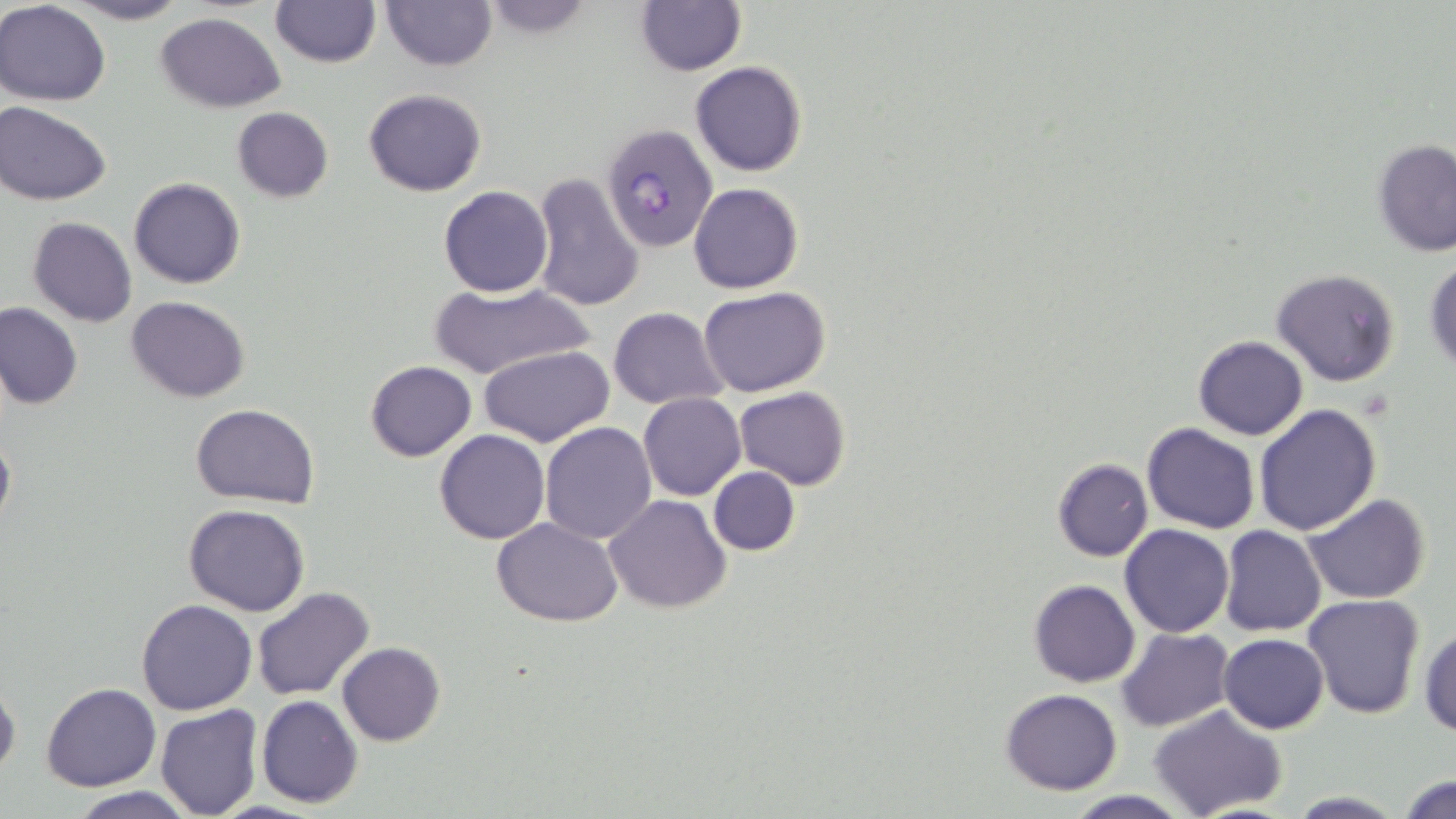

slide_level_diagnosis: Plasmodium falciparum
modality: optical microscopy
stain: May-Grünwald-Giemsa
preparation: thin blood smear
field_of_view: one of a larger specimen
uninfected_red_blood_cell_locations: 'approximate bounding boxes as named x1/y1/x2/y2 corners in pixels: (x1=64, y1=0, x2=191, y2=25), (x1=381, y1=0, x2=496, y2=70), (x1=1, y1=1, x2=113, y2=105), (x1=269, y1=1, x2=379, y2=68), (x1=634, y1=1, x2=746, y2=76), (x1=472, y1=2, x2=603, y2=37), (x1=155, y1=11, x2=287, y2=112), (x1=690, y1=61, x2=807, y2=176), (x1=364, y1=88, x2=487, y2=196), (x1=0, y1=101, x2=111, y2=205), (x1=231, y1=107, x2=333, y2=204), (x1=1372, y1=139, x2=1456, y2=256), (x1=530, y1=173, x2=644, y2=312), (x1=129, y1=177, x2=246, y2=289), (x1=688, y1=183, x2=804, y2=294), (x1=439, y1=186, x2=552, y2=297), (x1=26, y1=217, x2=137, y2=327), (x1=1424, y1=255, x2=1456, y2=375), (x1=1270, y1=268, x2=1402, y2=387), (x1=425, y1=281, x2=599, y2=381), (x1=699, y1=285, x2=832, y2=397), (x1=127, y1=295, x2=250, y2=402), (x1=0, y1=304, x2=83, y2=408), (x1=608, y1=307, x2=727, y2=409), (x1=1192, y1=335, x2=1308, y2=440), (x1=480, y1=344, x2=615, y2=448), (x1=364, y1=360, x2=477, y2=460), (x1=735, y1=386, x2=851, y2=490), (x1=638, y1=392, x2=746, y2=501), (x1=190, y1=403, x2=321, y2=507), (x1=1253, y1=405, x2=1382, y2=536), (x1=539, y1=422, x2=656, y2=543), (x1=1141, y1=423, x2=1261, y2=533), (x1=435, y1=429, x2=551, y2=544), (x1=0, y1=431, x2=15, y2=532), (x1=1053, y1=459, x2=1154, y2=561), (x1=707, y1=466, x2=800, y2=556), (x1=603, y1=493, x2=732, y2=613), (x1=1303, y1=493, x2=1432, y2=604), (x1=185, y1=504, x2=310, y2=616), (x1=492, y1=517, x2=623, y2=625), (x1=1120, y1=523, x2=1234, y2=636), (x1=1218, y1=526, x2=1326, y2=637), (x1=1030, y1=580, x2=1140, y2=687), (x1=253, y1=587, x2=375, y2=699), (x1=1302, y1=594, x2=1427, y2=720), (x1=137, y1=599, x2=256, y2=715), (x1=1419, y1=624, x2=1455, y2=738), (x1=1117, y1=628, x2=1234, y2=730), (x1=1218, y1=633, x2=1328, y2=733), (x1=337, y1=642, x2=445, y2=747), (x1=0, y1=680, x2=20, y2=779), (x1=42, y1=683, x2=161, y2=792), (x1=1000, y1=687, x2=1123, y2=795), (x1=256, y1=694, x2=363, y2=809), (x1=154, y1=703, x2=265, y2=819), (x1=1149, y1=705, x2=1289, y2=819), (x1=1396, y1=773, x2=1455, y2=819), (x1=65, y1=788, x2=199, y2=819), (x1=1060, y1=790, x2=1195, y2=819), (x1=1284, y1=791, x2=1409, y2=818)'
magnification: 1000x
plasmodium_falciparum_infected_red_blood_cell_locations: 'approximate bounding boxes as named x1/y1/x2/y2 corners in pixels: (x1=601, y1=121, x2=720, y2=253)'
image_size: 1456×819 pixels